Report the malaria status of this cell.
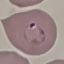

It is parasitized.

Cell patch, automatically extracted from a larger field of view and resized to 64 × 64 pixels. Giemsa stain. Acquired by smartphone through the microscope eyepiece. Thin blood film.